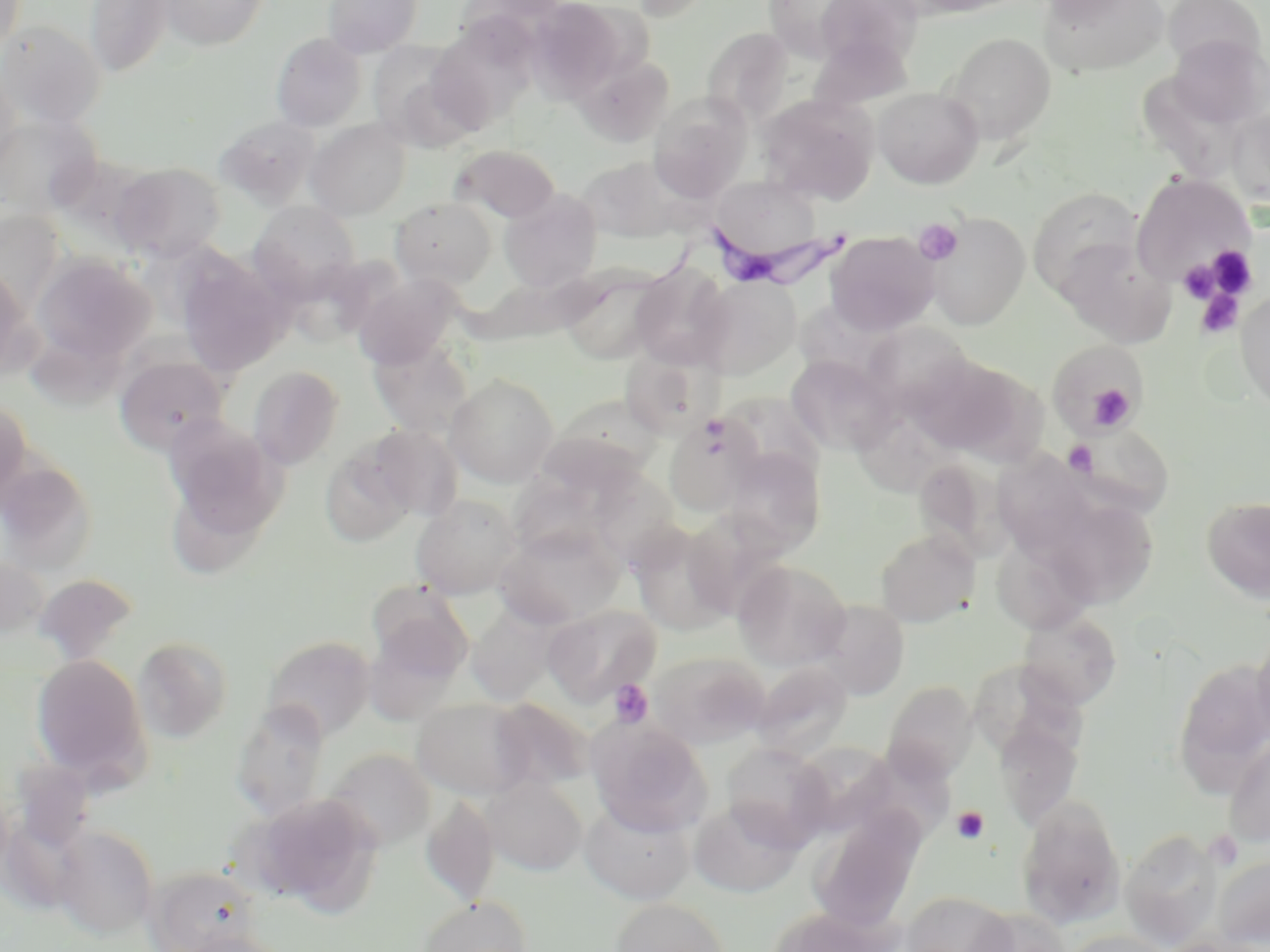

{
  "slide_level_diagnosis": "Trypanosoma brucei",
  "platelet_locations": "approximate bounding boxes as named x1/y1/x2/y2 corners in pixels: (x1=913, y1=218, x2=963, y2=265), (x1=1206, y1=245, x2=1256, y2=298), (x1=1179, y1=262, x2=1218, y2=302), (x1=1196, y1=288, x2=1245, y2=339), (x1=1087, y1=385, x2=1133, y2=427), (x1=1063, y1=441, x2=1097, y2=476), (x1=608, y1=679, x2=653, y2=728), (x1=952, y1=806, x2=989, y2=844)",
  "image_size": "1270×952 pixels",
  "stain": "May-Grünwald-Giemsa",
  "uninfected_red_blood_cell_locations": "approximate bounding boxes as named x1/y1/x2/y2 corners in pixels: (x1=0, y1=0, x2=26, y2=59), (x1=85, y1=0, x2=173, y2=77), (x1=158, y1=0, x2=269, y2=50), (x1=323, y1=0, x2=422, y2=58), (x1=622, y1=0, x2=714, y2=21), (x1=761, y1=0, x2=877, y2=64), (x1=814, y1=0, x2=925, y2=70), (x1=1038, y1=0, x2=1138, y2=23), (x1=1040, y1=0, x2=1171, y2=77), (x1=525, y1=1, x2=626, y2=102), (x1=1163, y1=1, x2=1267, y2=74), (x1=0, y1=20, x2=106, y2=129), (x1=427, y1=24, x2=534, y2=134), (x1=701, y1=26, x2=795, y2=125), (x1=270, y1=32, x2=367, y2=131), (x1=943, y1=32, x2=1056, y2=146), (x1=1166, y1=34, x2=1269, y2=129), (x1=367, y1=41, x2=483, y2=150), (x1=577, y1=55, x2=674, y2=146), (x1=0, y1=70, x2=22, y2=177), (x1=873, y1=87, x2=983, y2=189), (x1=758, y1=93, x2=879, y2=205), (x1=648, y1=94, x2=753, y2=201), (x1=1228, y1=107, x2=1270, y2=209), (x1=0, y1=113, x2=102, y2=218), (x1=215, y1=115, x2=319, y2=208), (x1=305, y1=119, x2=411, y2=220), (x1=450, y1=144, x2=560, y2=224), (x1=579, y1=156, x2=683, y2=243), (x1=110, y1=161, x2=227, y2=262), (x1=1130, y1=172, x2=1254, y2=287), (x1=708, y1=176, x2=821, y2=263), (x1=1028, y1=187, x2=1144, y2=297), (x1=498, y1=189, x2=602, y2=293), (x1=390, y1=196, x2=497, y2=289), (x1=248, y1=200, x2=361, y2=297), (x1=0, y1=210, x2=64, y2=312), (x1=924, y1=212, x2=1031, y2=330), (x1=825, y1=232, x2=939, y2=336), (x1=1054, y1=236, x2=1176, y2=346), (x1=31, y1=253, x2=156, y2=367), (x1=175, y1=255, x2=291, y2=377), (x1=0, y1=264, x2=33, y2=381), (x1=630, y1=264, x2=733, y2=369), (x1=558, y1=267, x2=670, y2=365), (x1=352, y1=272, x2=464, y2=369), (x1=695, y1=276, x2=800, y2=380), (x1=1236, y1=290, x2=1270, y2=412), (x1=867, y1=324, x2=976, y2=418), (x1=27, y1=333, x2=130, y2=418), (x1=367, y1=337, x2=474, y2=438), (x1=1047, y1=340, x2=1143, y2=435), (x1=620, y1=348, x2=717, y2=439), (x1=912, y1=353, x2=1041, y2=463), (x1=115, y1=354, x2=227, y2=454), (x1=785, y1=355, x2=898, y2=455), (x1=248, y1=365, x2=344, y2=469), (x1=445, y1=374, x2=559, y2=487), (x1=0, y1=396, x2=31, y2=509), (x1=552, y1=396, x2=663, y2=491), (x1=859, y1=404, x2=961, y2=502), (x1=664, y1=413, x2=762, y2=517), (x1=163, y1=415, x2=286, y2=541), (x1=1066, y1=421, x2=1175, y2=517), (x1=365, y1=424, x2=463, y2=521), (x1=521, y1=441, x2=638, y2=562), (x1=320, y1=445, x2=417, y2=548), (x1=998, y1=445, x2=1094, y2=560), (x1=723, y1=448, x2=826, y2=555), (x1=0, y1=458, x2=85, y2=580), (x1=916, y1=465, x2=1022, y2=565), (x1=586, y1=469, x2=684, y2=566), (x1=168, y1=490, x2=262, y2=574), (x1=411, y1=494, x2=523, y2=598), (x1=1202, y1=496, x2=1270, y2=601), (x1=1047, y1=500, x2=1158, y2=610), (x1=629, y1=522, x2=736, y2=635), (x1=496, y1=524, x2=627, y2=628), (x1=875, y1=528, x2=980, y2=627), (x1=0, y1=554, x2=49, y2=642), (x1=733, y1=560, x2=851, y2=669), (x1=33, y1=572, x2=139, y2=665), (x1=367, y1=582, x2=473, y2=685), (x1=812, y1=599, x2=909, y2=700), (x1=543, y1=604, x2=662, y2=706), (x1=466, y1=608, x2=558, y2=705), (x1=1018, y1=611, x2=1122, y2=709), (x1=1251, y1=630, x2=1270, y2=746), (x1=261, y1=635, x2=376, y2=740), (x1=133, y1=636, x2=234, y2=743), (x1=647, y1=651, x2=770, y2=748), (x1=30, y1=653, x2=150, y2=787), (x1=1172, y1=658, x2=1270, y2=786), (x1=750, y1=661, x2=853, y2=760), (x1=882, y1=680, x2=977, y2=784), (x1=412, y1=697, x2=533, y2=799), (x1=487, y1=698, x2=594, y2=793), (x1=231, y1=702, x2=330, y2=821), (x1=587, y1=718, x2=711, y2=834), (x1=994, y1=718, x2=1083, y2=829), (x1=1222, y1=733, x2=1270, y2=848), (x1=791, y1=740, x2=900, y2=836), (x1=721, y1=742, x2=832, y2=848), (x1=325, y1=749, x2=436, y2=851), (x1=10, y1=760, x2=95, y2=848), (x1=480, y1=776, x2=587, y2=876), (x1=250, y1=794, x2=384, y2=916), (x1=421, y1=795, x2=499, y2=907), (x1=1016, y1=795, x2=1127, y2=928), (x1=579, y1=797, x2=696, y2=904), (x1=689, y1=799, x2=805, y2=898), (x1=809, y1=809, x2=926, y2=932), (x1=54, y1=825, x2=159, y2=938), (x1=1120, y1=829, x2=1224, y2=948), (x1=1213, y1=855, x2=1270, y2=948), (x1=147, y1=865, x2=262, y2=952), (x1=902, y1=890, x2=1015, y2=952), (x1=416, y1=896, x2=533, y2=952), (x1=610, y1=898, x2=730, y2=952), (x1=767, y1=905, x2=895, y2=952), (x1=969, y1=908, x2=1070, y2=952), (x1=180, y1=929, x2=294, y2=952), (x1=1059, y1=930, x2=1175, y2=952)",
  "field_of_view": "one of a larger specimen",
  "trypanosoma_brucei_locations": "approximate bounding boxes as named x1/y1/x2/y2 corners in pixels: (x1=586, y1=212, x2=859, y2=315)",
  "modality": "light microscopy",
  "magnification": "1000x",
  "preparation": "thin blood smear"
}